Assess the morphology of the red blood cells.
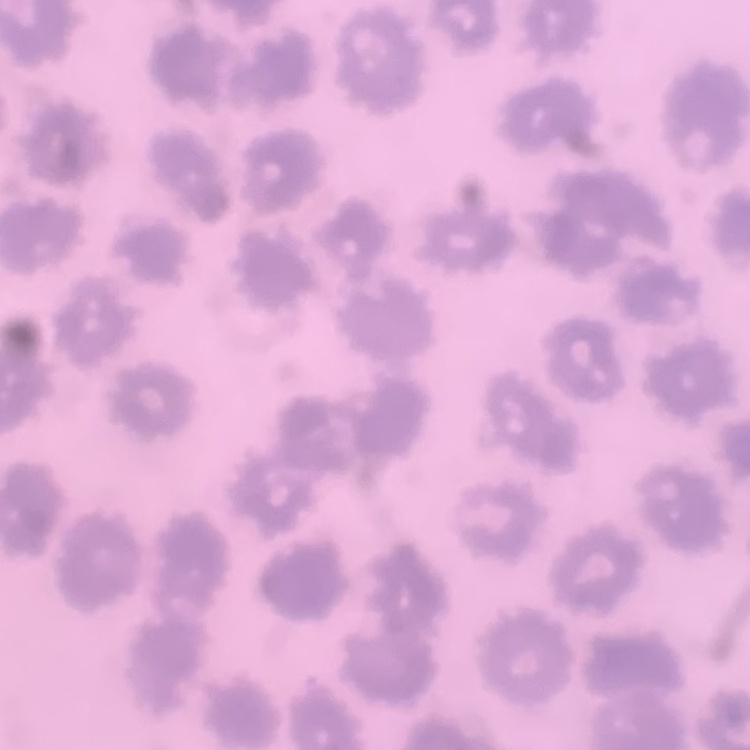
No rouleaux formation.

One tile cut from a larger photomicrograph. Field's or Giemsa stain. Thin blood smear.